Classify this cell by malaria status.
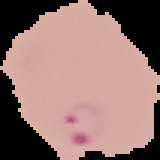

It is parasitized.

image size = 160×160 pixels
preparation = thin blood film
image type = segmented cell region with the area outside set to black